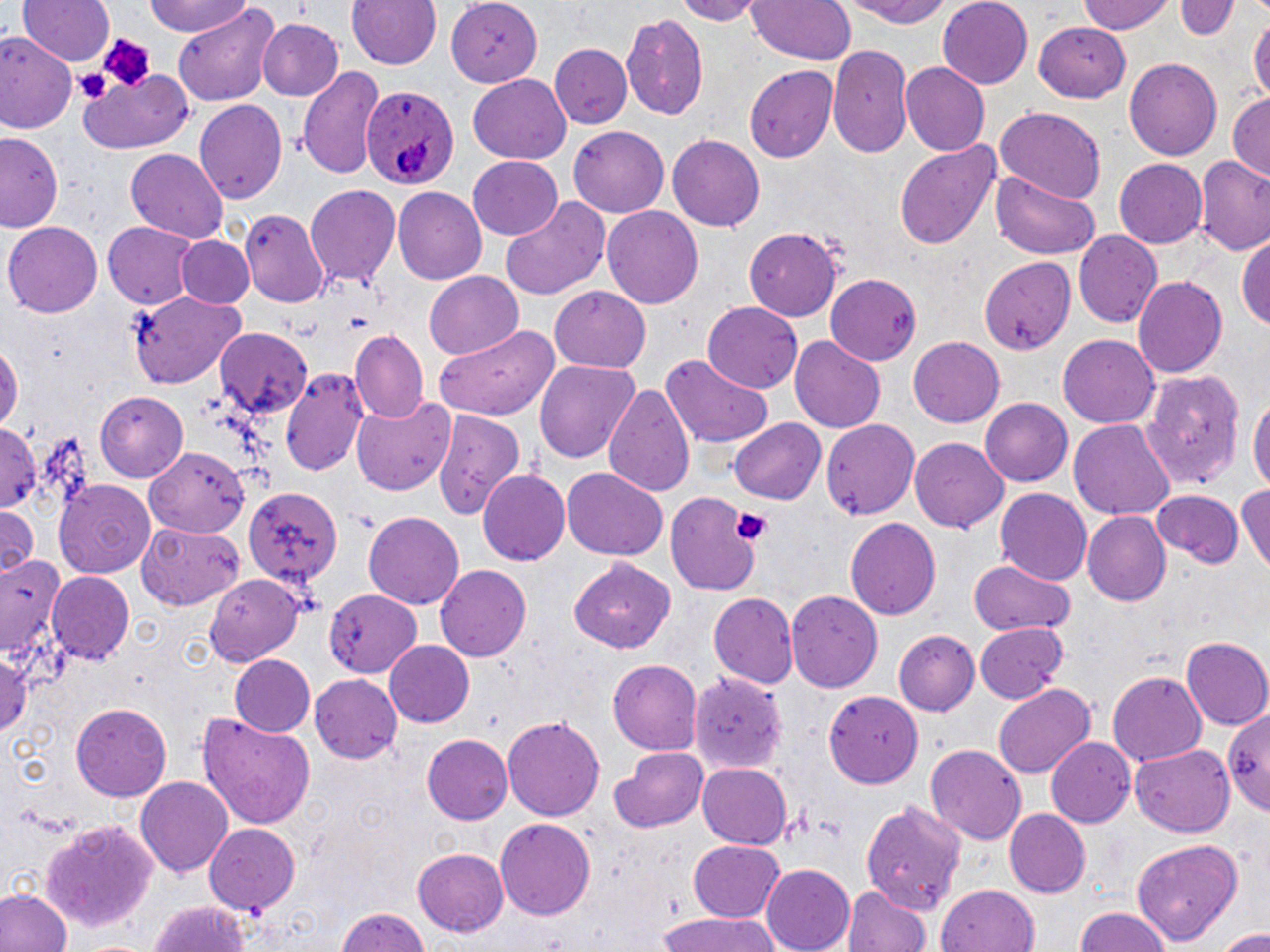
Summary:
  - Coordinate format: approximate bounding boxes as [x1, y1, x2, y2] in pixels
  - Plasmodium ovale-infected red blood cell locations: [361, 86, 456, 193]
  - Uninfected red blood cell locations: [20, 0, 115, 69], [146, 0, 254, 37], [348, 0, 441, 71], [668, 0, 765, 23], [745, 0, 856, 64], [833, 0, 962, 27], [938, 0, 1034, 89], [1079, 0, 1176, 35], [1176, 0, 1237, 42], [448, 1, 543, 85], [172, 5, 278, 107], [1248, 11, 1269, 114], [620, 14, 712, 118], [258, 19, 344, 101], [1036, 22, 1133, 101], [1, 32, 77, 135], [551, 46, 632, 129], [828, 46, 914, 160], [1123, 57, 1222, 160], [899, 61, 991, 156], [294, 64, 385, 179], [746, 66, 838, 163], [78, 71, 192, 155], [468, 74, 572, 163], [1228, 94, 1269, 183], [195, 97, 288, 204], [991, 106, 1106, 204], [568, 127, 670, 214], [1, 131, 64, 235], [668, 135, 765, 229], [895, 139, 1003, 250], [125, 147, 228, 244], [467, 156, 564, 240], [1194, 158, 1270, 254], [1114, 160, 1207, 249], [986, 167, 1103, 261], [306, 185, 401, 287], [394, 188, 487, 286], [500, 200, 608, 299], [603, 206, 704, 308], [240, 209, 328, 308], [4, 219, 103, 315], [103, 223, 197, 309], [744, 227, 845, 319], [1237, 230, 1270, 335], [1074, 231, 1162, 330], [175, 235, 254, 310], [975, 255, 1080, 356], [423, 271, 524, 359], [824, 273, 922, 363], [1133, 274, 1229, 382], [548, 286, 653, 373], [128, 289, 247, 389], [702, 302, 803, 393], [432, 325, 562, 419], [214, 328, 313, 415], [350, 330, 429, 424], [1057, 333, 1159, 427], [908, 336, 1005, 426], [790, 337, 884, 433], [0, 339, 24, 437], [660, 353, 775, 450], [536, 360, 640, 463], [281, 366, 369, 479], [1137, 368, 1249, 487], [605, 380, 696, 501], [1249, 388, 1270, 500], [97, 392, 188, 480], [352, 397, 455, 496], [978, 398, 1071, 486], [430, 408, 523, 523], [0, 419, 42, 511], [730, 419, 825, 504], [822, 419, 922, 522], [1069, 420, 1176, 523], [910, 437, 1008, 532], [143, 446, 251, 538], [563, 467, 666, 560], [480, 468, 571, 565], [55, 481, 157, 577], [1235, 481, 1270, 575], [244, 487, 343, 591], [1151, 487, 1246, 570], [993, 488, 1093, 586], [666, 489, 763, 595], [0, 504, 40, 575], [1081, 511, 1172, 607], [362, 512, 465, 610], [845, 517, 941, 620], [137, 520, 246, 609], [0, 553, 66, 676], [570, 557, 677, 653], [968, 558, 1073, 636], [435, 564, 531, 664], [205, 565, 307, 664], [46, 570, 133, 662], [325, 586, 420, 678], [787, 589, 883, 691], [708, 592, 798, 688], [975, 622, 1067, 704], [897, 630, 980, 717], [1182, 637, 1270, 729], [385, 641, 474, 726], [0, 646, 35, 745], [231, 656, 316, 738], [608, 659, 702, 754], [1108, 669, 1209, 769], [692, 671, 786, 774], [311, 674, 402, 764], [992, 684, 1097, 777], [825, 689, 922, 790], [1224, 701, 1270, 810], [69, 702, 171, 802], [198, 711, 317, 828], [503, 713, 605, 822], [421, 733, 513, 824], [1047, 738, 1133, 828], [925, 742, 1027, 844], [1129, 743, 1234, 839], [612, 745, 707, 833], [697, 763, 792, 849], [135, 774, 232, 874], [858, 792, 965, 915], [1003, 808, 1090, 897], [37, 818, 159, 935], [495, 818, 596, 922], [205, 824, 299, 915], [1134, 836, 1247, 945], [687, 841, 787, 921], [412, 848, 509, 938], [761, 862, 856, 952], [845, 883, 933, 952], [936, 885, 1042, 952], [0, 888, 72, 952], [148, 900, 253, 952], [333, 906, 434, 952], [1074, 906, 1173, 952], [654, 912, 779, 952], [1216, 928, 1270, 951]
  - Platelet locations: [94, 31, 157, 90], [73, 65, 113, 106], [733, 508, 771, 544]
  - Slide-level diagnosis: Plasmodium ovale
  - Magnification: 1000x
  - Preparation: thin blood smear
  - Modality: light microscopy
  - Image size: 1270×952 pixels
  - Field of view: single
  - Stain: May-Grünwald-Giemsa